Find each parasitized RBC.
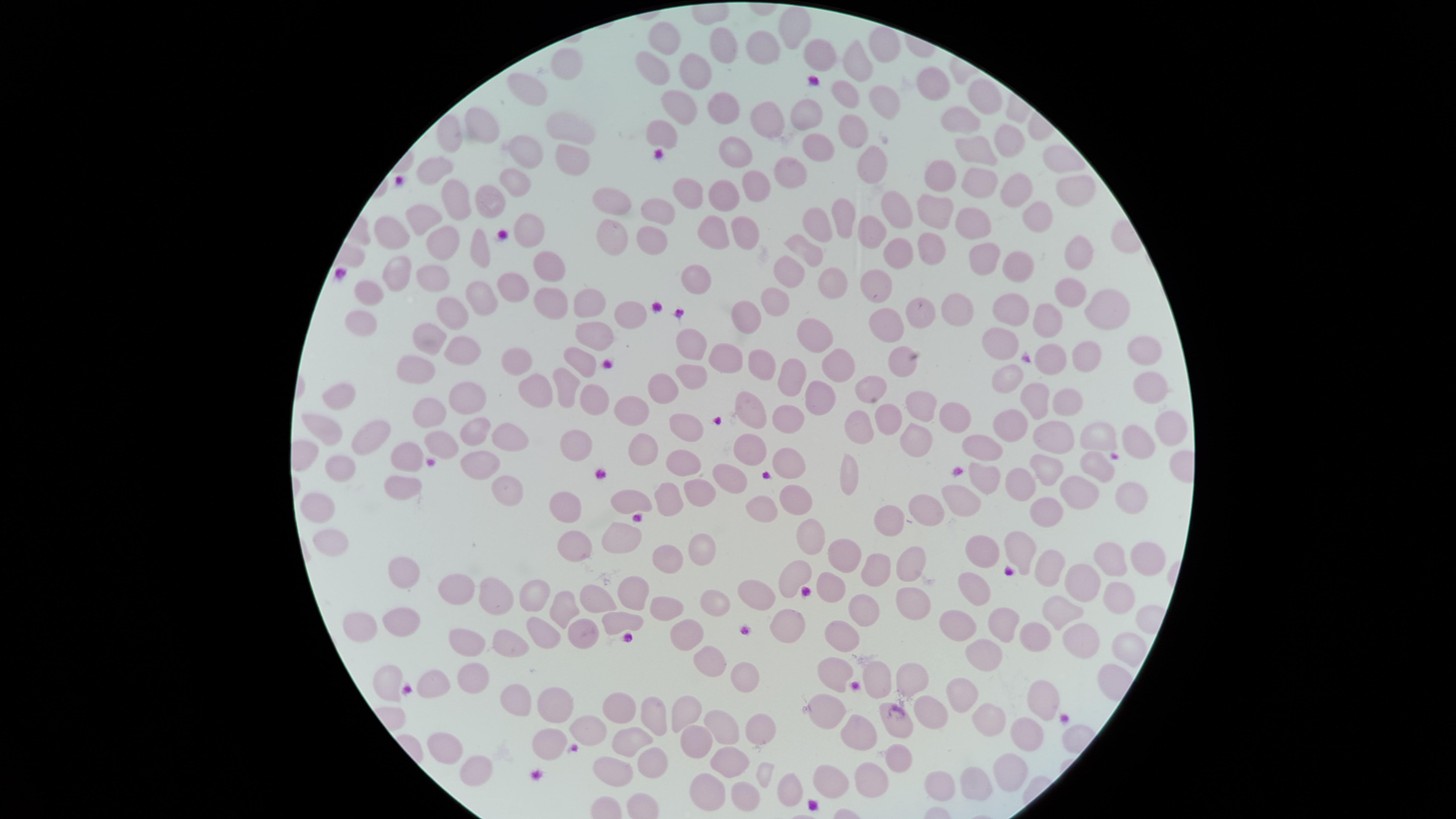

No parasitized RBCs identified.

Approximate marker points as {x, y} in pixels.
Summary:
  - Uninfected RBCs: {789, 31}, {661, 36}, {719, 47}, {886, 47}, {761, 53}, {814, 56}, {559, 64}, {651, 66}, {698, 66}, {860, 66}, {937, 84}, {527, 90}, {843, 90}, {978, 101}, {879, 102}, {800, 109}, {679, 110}, {966, 115}, {765, 122}, {485, 126}, {563, 128}, {449, 134}, {658, 134}, {853, 134}, {1009, 136}, {818, 144}, {970, 147}, {523, 155}, {733, 155}, {570, 158}, {870, 162}, {1061, 162}, {438, 163}, {786, 173}, {936, 176}, {512, 178}, {985, 183}, {1069, 188}, {752, 190}, {688, 191}, {723, 193}, {451, 195}, {1018, 195}, {618, 203}, {894, 206}, {491, 207}, {658, 211}, {932, 213}, {843, 216}, {425, 217}, {1031, 220}, {819, 222}, {969, 222}, {740, 226}, {395, 227}, {875, 227}, {530, 228}, {711, 233}, {652, 234}, {445, 240}, {611, 241}, {804, 245}, {934, 246}, {478, 249}, {1081, 250}, {895, 255}, {985, 256}, {548, 263}, {1022, 267}, {393, 275}, {428, 275}, {791, 275}, {698, 280}, {829, 281}, {878, 286}, {374, 289}, {1067, 289}, {512, 290}, {476, 296}, {587, 296}, {776, 296}, {956, 306}, {554, 307}, {1016, 307}, {1099, 307}, {920, 308}, {633, 311}, {452, 313}, {744, 315}, {1052, 321}, {361, 324}, {887, 328}, {815, 330}, {432, 333}, {588, 335}, {1005, 339}, {691, 343}, {1147, 349}, {463, 355}, {1091, 355}, {902, 358}, {1052, 358}, {578, 359}, {719, 360}, {761, 365}, {835, 365}, {416, 367}, {515, 367}, {690, 376}, {793, 376}, {1009, 379}, {1148, 386}, {667, 388}, {568, 391}, {874, 391}, {534, 392}, {471, 397}, {1039, 398}, {344, 400}, {598, 400}, {1072, 402}, {427, 404}, {819, 404}, {925, 404}, {632, 409}, {750, 413}, {952, 413}, {786, 416}, {886, 416}, {1011, 419}, {1170, 422}, {320, 425}, {683, 427}, {468, 429}, {860, 429}, {511, 434}, {918, 436}, {1050, 436}, {442, 438}, {1143, 438}, {1103, 439}, {367, 440}, {578, 442}, {982, 449}, {403, 451}, {642, 451}, {744, 452}, {336, 463}, {475, 463}, {678, 463}, {787, 467}, {1099, 468}, {1051, 471}, {849, 473}, {399, 474}, {992, 476}, {726, 481}, {503, 487}, {1014, 487}, {696, 494}, {1129, 496}, {963, 497}, {1077, 497}, {634, 499}, {787, 499}, {667, 500}, {316, 504}, {569, 508}, {762, 508}, {929, 508}, {1046, 516}, {892, 521}, {814, 532}, {620, 537}, {705, 538}, {585, 539}, {328, 542}, {844, 550}, {982, 552}, {1014, 552}, {667, 555}, {1149, 558}, {1108, 561}, {908, 565}, {792, 566}, {1045, 566}, {399, 569}, {876, 570}, {1077, 584}, {461, 588}, {630, 589}, {498, 590}, {979, 590}, {830, 591}, {761, 595}, {1118, 595}, {539, 596}, {596, 597}, {713, 600}, {912, 605}, {556, 606}, {664, 607}, {867, 609}, {1067, 609}, {999, 613}, {365, 619}, {614, 624}, {787, 624}, {391, 626}, {958, 629}, {1033, 631}, {545, 632}, {680, 637}, {846, 637}, {578, 638}, {515, 640}, {473, 644}, {1085, 644}, {1121, 647}, {980, 651}, {709, 660}, {876, 670}, {476, 679}, {747, 679}, {902, 679}, {833, 681}, {959, 694}, {1039, 698}, {557, 706}, {511, 708}, {686, 711}, {614, 712}, {834, 714}, {987, 715}, {651, 719}, {897, 722}, {761, 727}, {724, 728}, {585, 732}, {1024, 733}, {861, 734}, {629, 740}, {691, 740}, {449, 746}, {544, 746}, {895, 755}, {649, 760}, {729, 763}, {475, 769}, {606, 774}, {828, 776}, {867, 779}, {979, 779}, {1009, 781}, {939, 782}, {789, 788}, {699, 790}, {739, 797}
  - Capture: smartphone photograph through the microscope eyepiece
  - Image size: 1456×819 pixels
  - Visible region: circular
  - Field of view: single
  - Stain: Giemsa
  - Preparation: thin blood smear